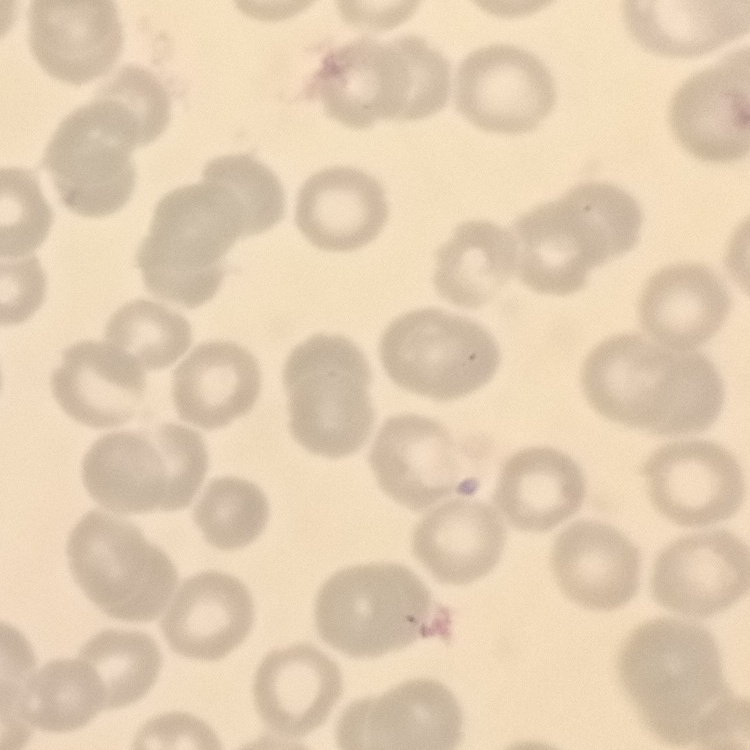

erythrocyte_morphology: no rouleaux formation
preparation: thin blood film
image_type: one tile cut from a larger photomicrograph
stain: Field's or Giemsa